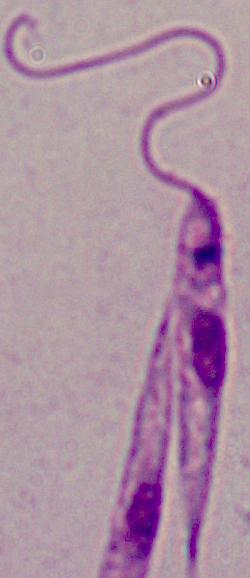

A Leishmania parasite is seen. Captured at 1000x magnification. Photomicrograph.